Describe the morphology of the erythrocytes.
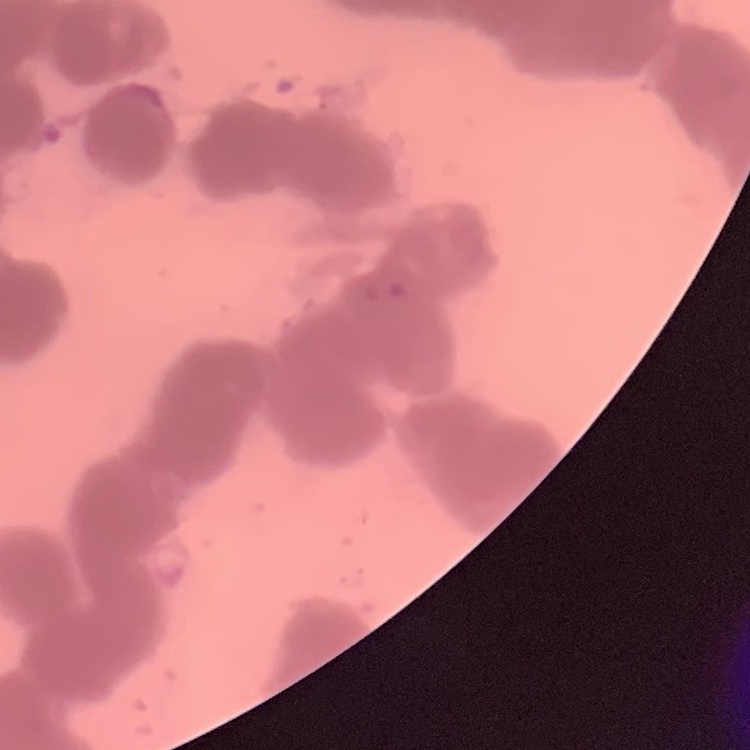

They show rouleaux formation.

{
  "stain": "Field's or Giemsa",
  "image_type": "square crop of a larger photomicrograph",
  "preparation": "thin blood film"
}